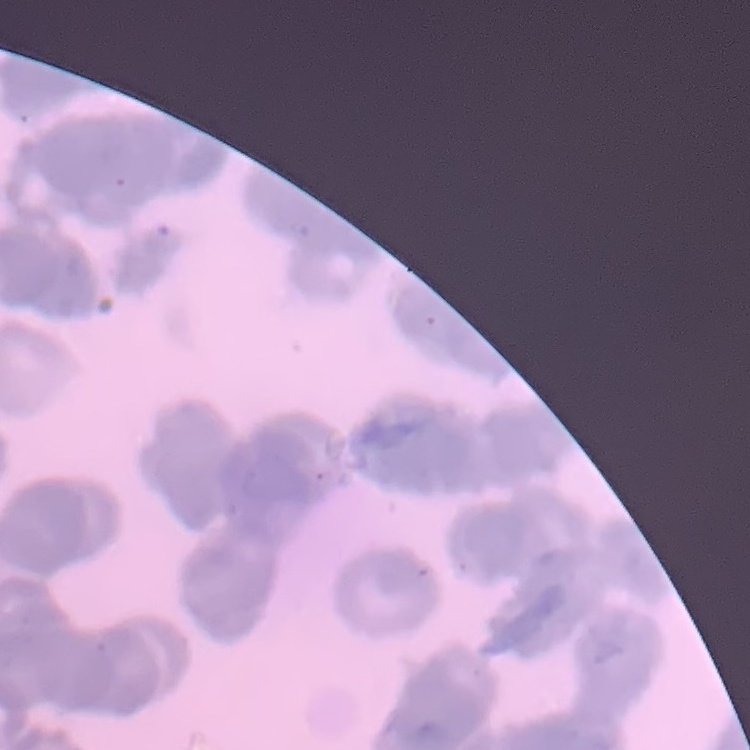

red blood cell morphology = rouleaux formation
image type = square crop of a larger photomicrograph
preparation = thin peripheral smear
stain = Field's or Giemsa